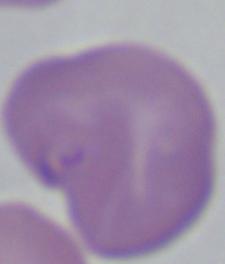
Photomicrograph. 1000x magnification. A Babesia parasite is seen.